Report the malaria status of this cell.
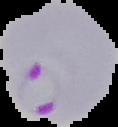

Parasitized.

Summary:
  - Preparation: thin blood film
  - Image type: segmented cell region on a black background
  - Image size: 118×127 pixels